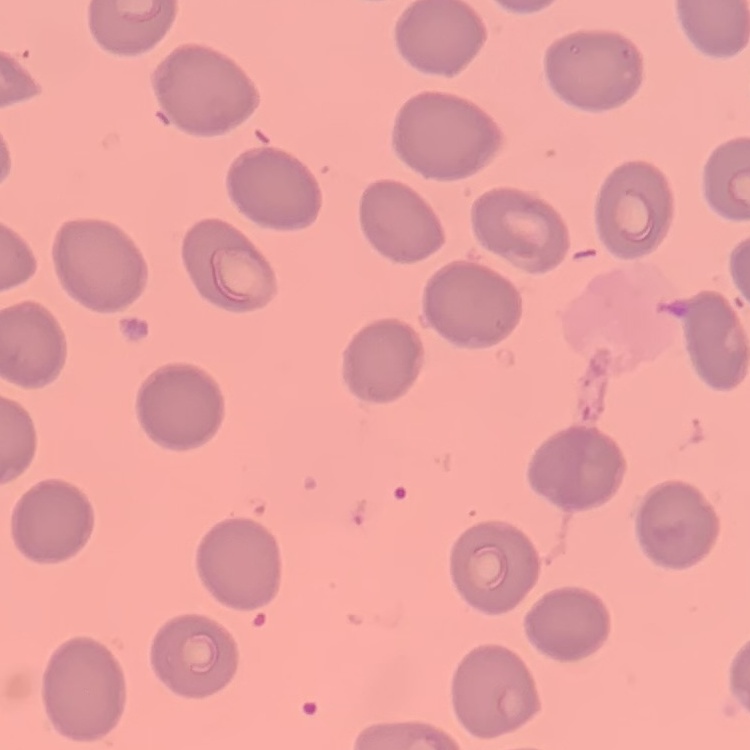

Summary:
  - Red blood cell morphology: no rouleaux formation
  - Image type: one tile cut from a larger photomicrograph
  - Preparation: thin blood film
  - Stain: Field's or Giemsa